Outline each Plasmodium falciparum-infected red blood cell.
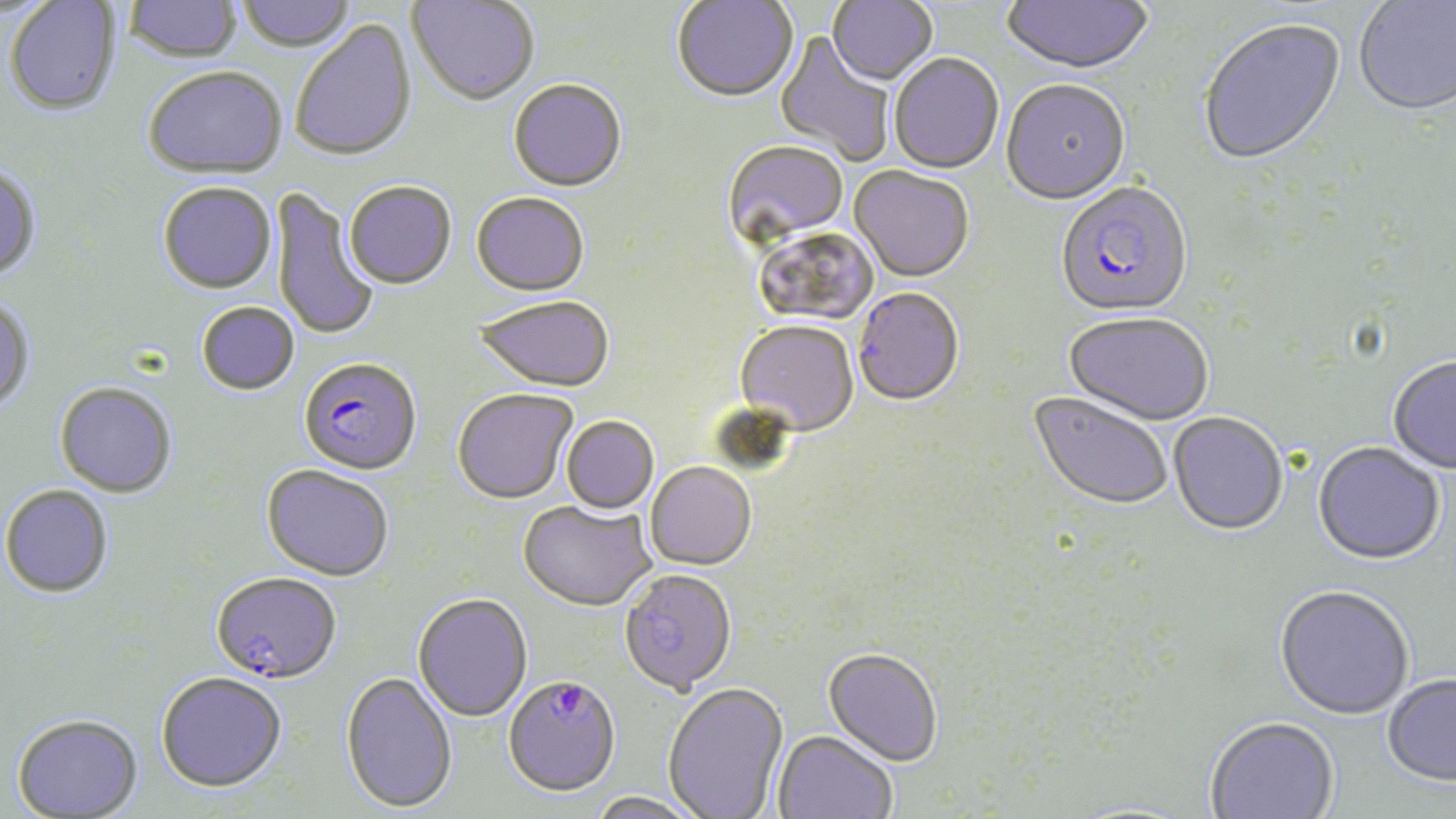
Approximate bounding boxes as (x1,y1)-(x2,y2) corner pairs in pixels.
Plasmodium falciparum-infected red blood cells: (1055,185)-(1193,320), (852,290)-(964,409), (298,360)-(422,478), (211,575)-(341,687), (503,677)-(621,800).

slide-level diagnosis = Plasmodium falciparum
stain = May-Grünwald-Giemsa
field of view = one of a larger specimen
modality = optical microscopy
uninfected red blood cell locations = approximate bounding boxes as (x1,y1)-(x2,y2) corner pairs in pixels: (236,0)-(356,55), (408,0)-(539,109), (827,0)-(938,88), (1002,0)-(1153,77), (1354,0)-(1456,119), (5,1)-(121,118), (124,1)-(243,66), (672,1)-(798,105), (1198,19)-(1347,169), (291,20)-(418,165), (774,32)-(895,165), (889,55)-(1004,175), (143,69)-(288,183), (509,81)-(627,194), (1001,82)-(1131,207), (722,141)-(849,251), (0,165)-(42,284), (848,166)-(974,285), (345,184)-(457,292), (158,185)-(277,296), (270,189)-(379,342), (471,194)-(589,299), (755,226)-(880,327), (0,298)-(35,416), (474,298)-(614,395), (197,303)-(299,397), (1063,314)-(1213,428), (734,322)-(859,440), (1387,358)-(1456,475), (54,384)-(176,500), (452,390)-(578,507), (1027,392)-(1173,514), (1167,414)-(1288,538), (561,417)-(659,515), (1312,444)-(1445,567), (645,463)-(757,572), (261,467)-(393,583), (1,486)-(114,600), (517,501)-(655,614), (618,571)-(738,698), (1274,588)-(1413,722), (413,595)-(533,723), (822,650)-(942,769), (340,673)-(458,815), (155,674)-(287,796), (1381,677)-(1456,789), (663,684)-(789,819), (11,715)-(143,818), (1205,719)-(1340,818), (773,732)-(896,819), (585,793)-(707,819)
magnification = 1000x
preparation = thin blood film
image size = 1456×819 pixels